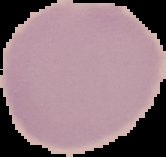

Summary:
  - Preparation: thin blood film
  - Result: no malaria parasites detected
  - Image type: segmented cell region on a black background
  - Image size: 166×157 pixels